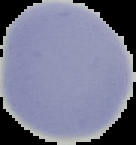 Result: no Plasmodium parasites seen. Image is 136×145 pixels. Segmented cell region on a black background. From a thin blood film.